Report the malaria status of this cell.
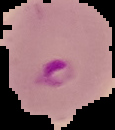
It is parasitized.

image type = cell region segmented out of the field of view; surrounding area masked to black
image size = 115×130 pixels
preparation = thin blood smear